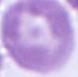
Micrograph. A red blood cell is seen. Captured at 1000x magnification.